State the preparation type.
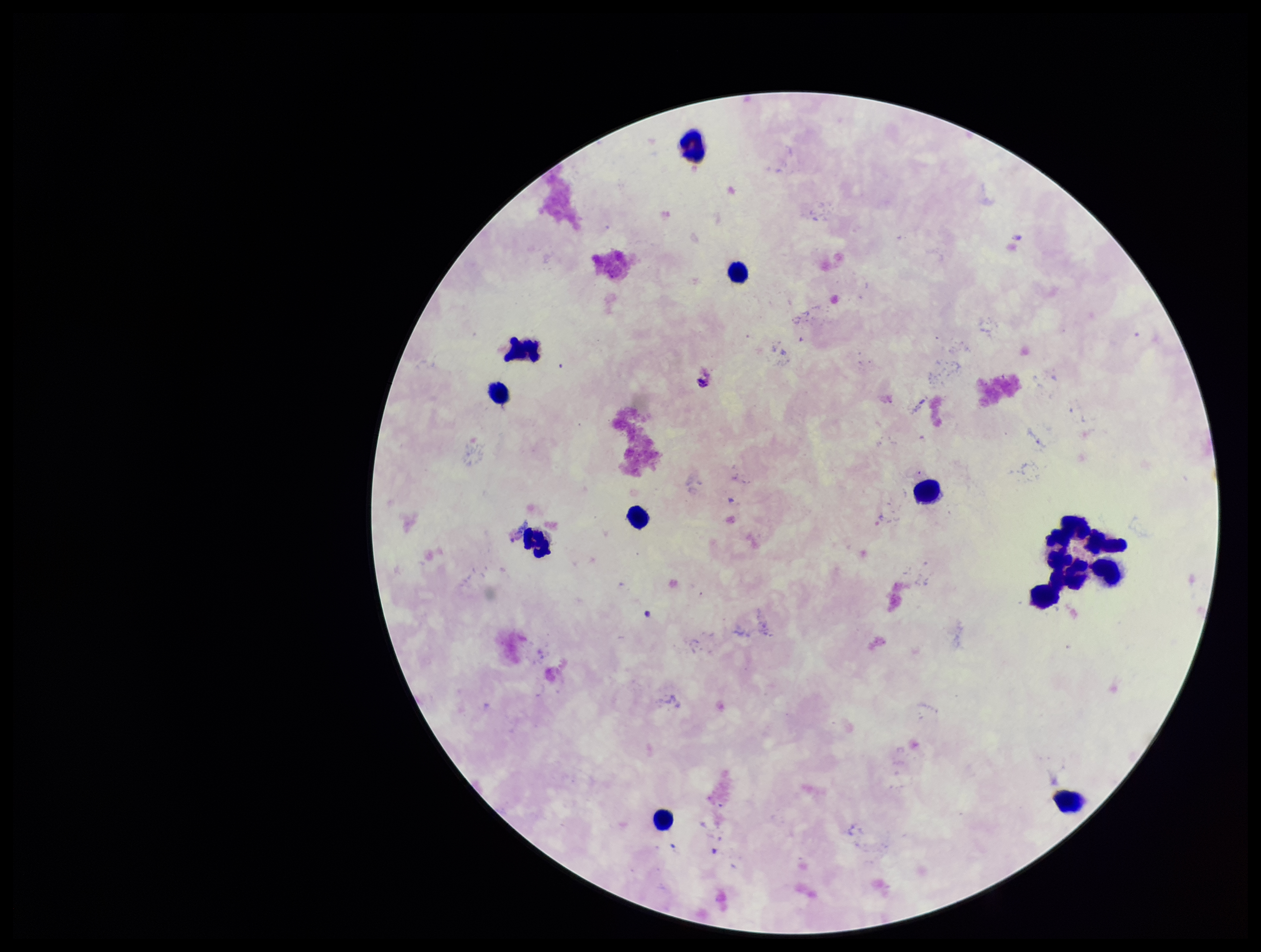
It is a thick blood smear.

Plasmodium parasites: none identified. Single field of view. Parasite count: 0. Leukocyte count: 14. Image is 1261×952 pixels. Photographed through the microscope eyepiece with a smartphone camera. Giemsa stain. Patient malaria status: negative.